Outline each blood parasite and name the species.
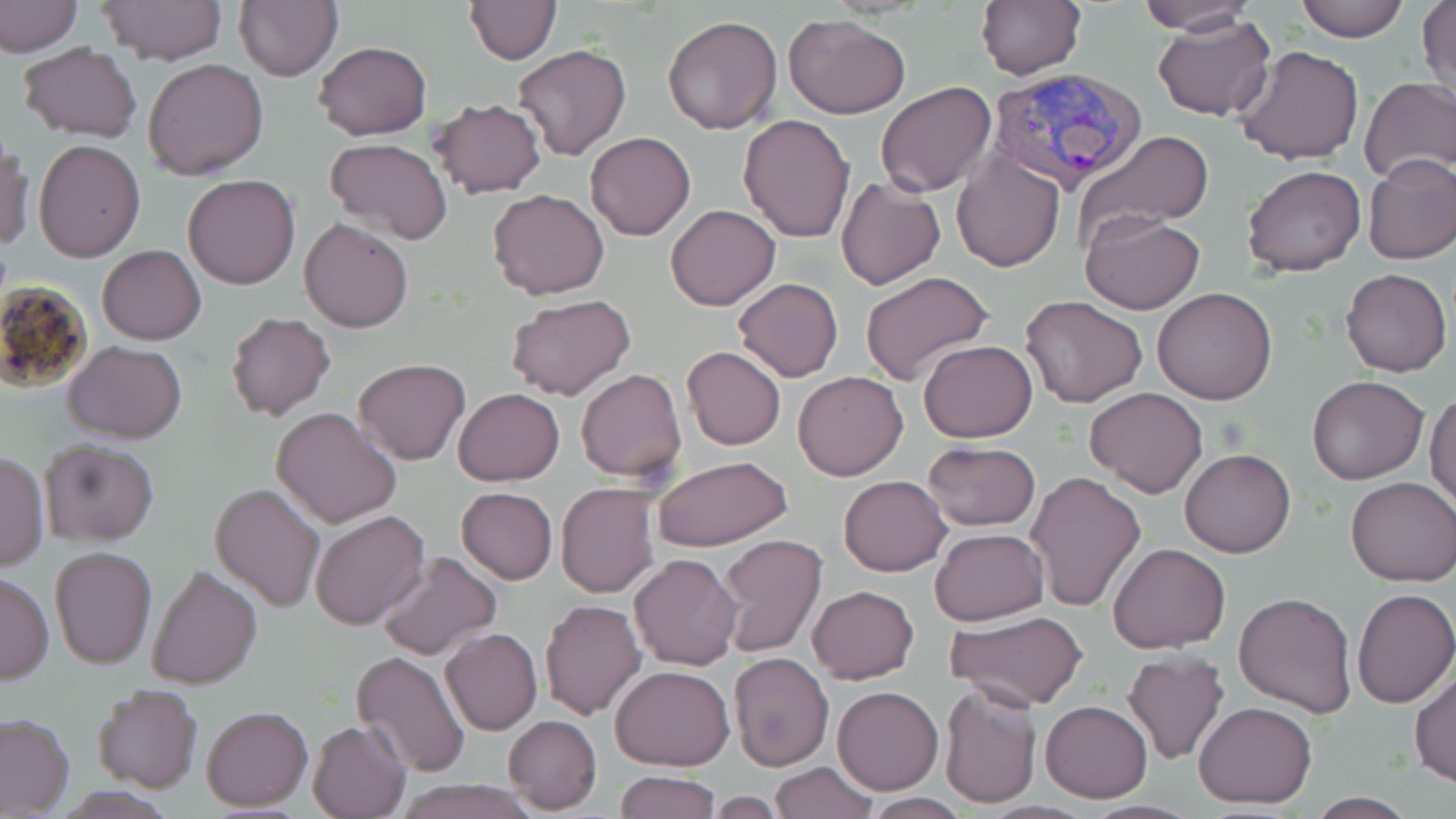
Approximate bounding boxes as [x1, y1, x2, y2] in pixels.
Plasmodium vivax-infected red blood cells: [988, 65, 1149, 197].
No Plasmodium falciparum, Plasmodium ovale, Plasmodium malariae, Babesia divergens, or Trypanosoma brucei observed.

slide-level diagnosis = Plasmodium vivax
preparation = thin blood smear
stain = May-Grünwald-Giemsa
modality = optical microscopy
magnification = 1000x
image size = 1456×819 pixels
uninfected red blood cell locations = approximate bounding boxes as [x1, y1, x2, y2] in pixels: [1, 0, 80, 56], [99, 0, 225, 65], [234, 0, 342, 82], [465, 0, 560, 63], [975, 0, 1085, 82], [1133, 0, 1261, 35], [1292, 0, 1411, 43], [1417, 0, 1454, 99], [1151, 13, 1276, 122], [662, 14, 783, 136], [784, 16, 911, 120], [313, 40, 432, 141], [17, 41, 143, 143], [513, 44, 632, 162], [1235, 45, 1365, 166], [143, 58, 269, 180], [1359, 77, 1456, 184], [876, 82, 998, 199], [428, 98, 546, 199], [738, 113, 855, 243], [1073, 130, 1216, 244], [586, 132, 695, 240], [0, 137, 33, 253], [33, 138, 146, 262], [324, 139, 453, 244], [951, 150, 1066, 273], [1363, 153, 1456, 265], [1242, 165, 1366, 278], [183, 174, 300, 290], [835, 174, 946, 290], [487, 187, 609, 300], [665, 204, 780, 311], [1080, 211, 1205, 314], [299, 217, 415, 334], [98, 244, 206, 345], [1340, 268, 1452, 376], [860, 272, 993, 388], [732, 278, 845, 383], [1153, 286, 1276, 404], [506, 294, 636, 401], [1020, 294, 1148, 408], [226, 312, 336, 421], [918, 339, 1039, 443], [65, 341, 187, 444], [682, 346, 786, 450], [353, 359, 470, 465], [576, 368, 686, 480], [793, 371, 909, 481], [1307, 374, 1429, 485], [1085, 387, 1208, 498], [452, 388, 564, 487], [1426, 389, 1456, 511], [271, 407, 401, 529], [39, 439, 159, 546], [921, 441, 1042, 532], [1179, 449, 1295, 558], [1, 452, 49, 572], [651, 455, 794, 553], [1024, 471, 1147, 614], [839, 475, 951, 576], [1347, 477, 1456, 588], [209, 482, 324, 613], [556, 483, 659, 599], [457, 487, 557, 583], [311, 510, 430, 629], [930, 528, 1049, 626], [716, 534, 828, 657], [1107, 542, 1232, 653], [51, 546, 157, 667], [375, 551, 501, 661], [627, 553, 744, 671], [146, 564, 263, 689], [0, 572, 53, 685], [807, 584, 918, 683], [1351, 588, 1456, 708], [1234, 590, 1359, 716], [540, 599, 646, 720], [942, 610, 1091, 713], [441, 627, 542, 735], [1120, 650, 1230, 765], [350, 651, 470, 777], [727, 653, 835, 772], [611, 664, 734, 771], [1410, 666, 1456, 786], [93, 683, 203, 793], [938, 684, 1041, 809], [833, 686, 942, 794], [1041, 700, 1152, 802], [1194, 701, 1317, 810], [200, 705, 312, 811], [0, 713, 77, 816], [503, 715, 602, 814], [307, 720, 410, 818], [768, 761, 878, 819], [615, 771, 721, 818], [389, 779, 538, 819], [1306, 794, 1422, 818], [858, 795, 974, 819], [1081, 800, 1201, 818]
field of view = one of a larger specimen